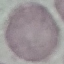
Summary:
  - Malaria status: uninfected
  - Capture: smartphone through the microscope eyepiece
  - Preparation: thin blood film
  - Stain: Giemsa
  - Image type: automatically extracted cell patch, resized to 64 × 64 pixels